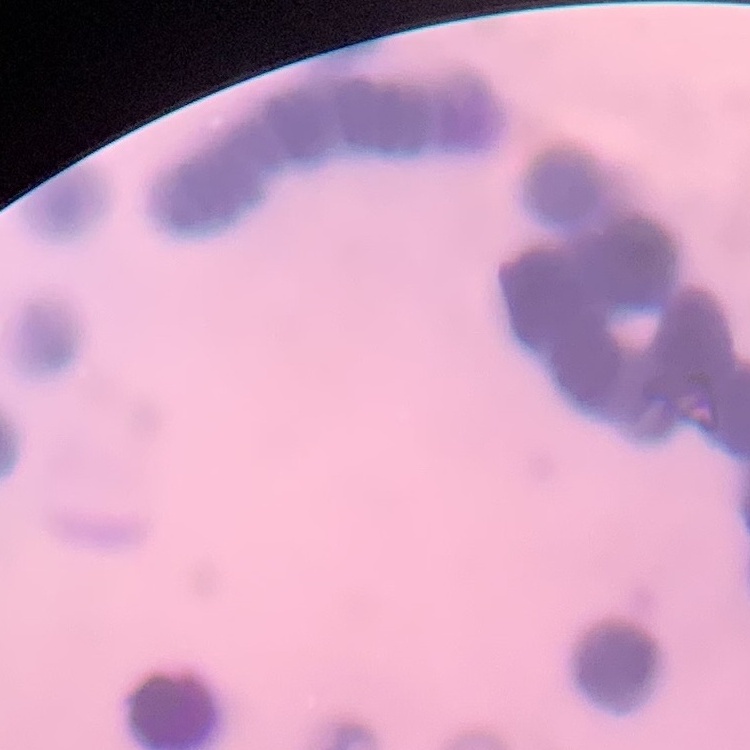

{
  "erythrocyte_morphology": "rouleaux formation",
  "image_type": "square crop of a larger photomicrograph",
  "stain": "Field's or Giemsa",
  "preparation": "thin blood smear"
}